Give the position of every malaria parasite.
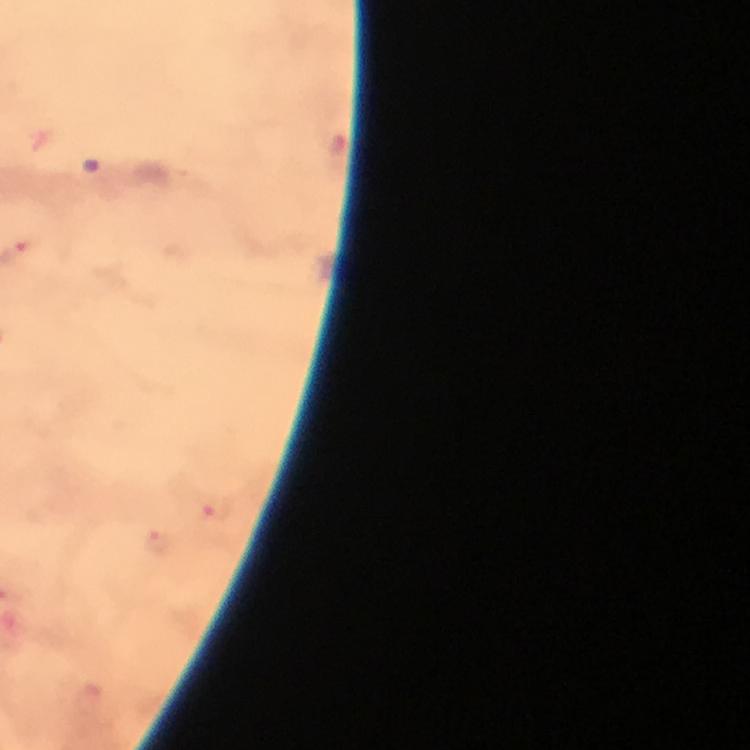
Approximate centers as [x, y] in pixels.
Malaria parasites: [218, 510], [158, 542].

context = from a malaria diagnostic workup
cropped from = one field of view
magnification = 100x
stain = Giemsa
immersion oil = used
preparation = thick smear
capture = smartphone photograph through a microscope
image size = 750×750 pixels